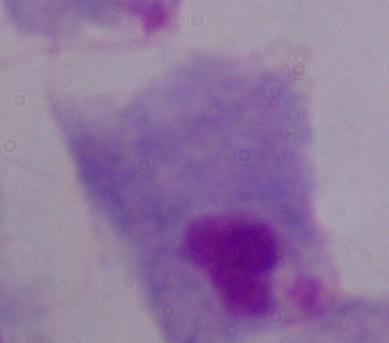

identification = trichomonad
modality = micrograph
magnification = 1000x